Report the malaria status of this cell.
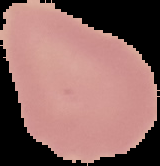

It is uninfected.

Summary:
  - Image size: 160×166 pixels
  - Image type: segmented cell region with the area outside set to black
  - Preparation: thin blood smear